Identify the cell.
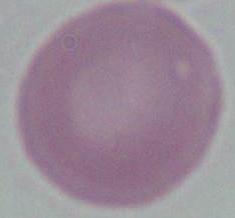
This is an erythrocyte.

Micrograph. Captured at 1000x magnification.